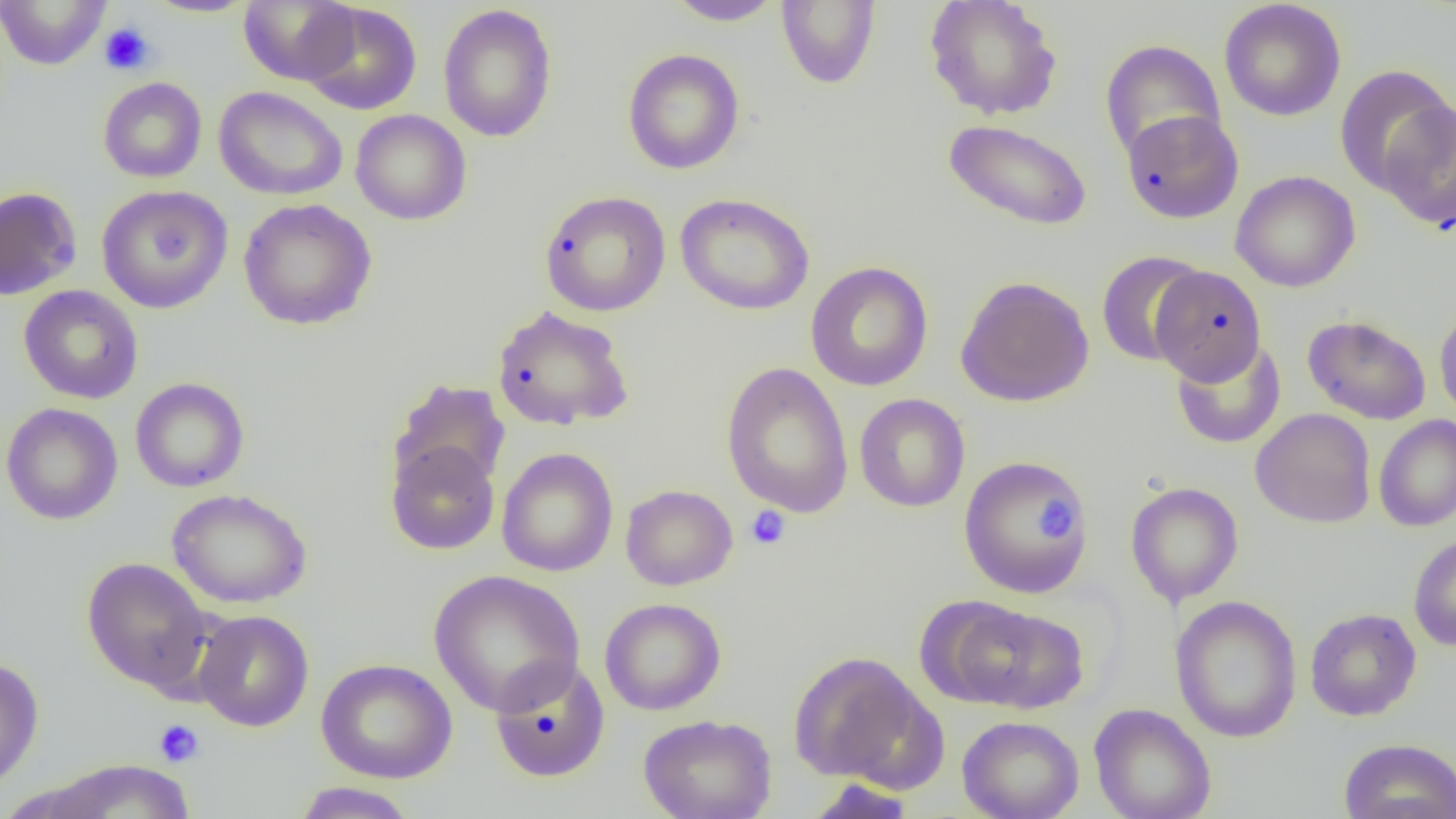

Summary:
  - Coordinate format: approximate bounding boxes as (x1, y1, x2, y2) in pixels
  - Uninfected red blood cell locations: (0, 0, 113, 70), (144, 0, 255, 17), (238, 0, 359, 85), (776, 0, 881, 90), (924, 0, 1063, 121), (665, 1, 786, 26), (1218, 1, 1347, 122), (299, 3, 422, 115), (438, 5, 558, 143), (1099, 39, 1226, 162), (622, 48, 745, 175), (1334, 64, 1454, 196), (97, 76, 207, 183), (214, 86, 348, 201), (1380, 101, 1456, 232), (350, 109, 472, 225), (1121, 110, 1244, 224), (942, 119, 1093, 232), (1230, 170, 1361, 292), (96, 185, 233, 313), (0, 186, 82, 301), (540, 191, 671, 317), (674, 193, 815, 316), (238, 198, 377, 330), (1096, 250, 1208, 367), (805, 261, 933, 391), (1151, 264, 1266, 385), (955, 276, 1094, 407), (18, 285, 143, 404), (1434, 304, 1456, 423), (491, 305, 635, 431), (1302, 314, 1432, 425), (1170, 337, 1286, 450), (721, 362, 853, 518), (130, 377, 249, 493), (388, 379, 510, 493), (854, 393, 970, 512), (1, 403, 123, 525), (1250, 408, 1377, 528), (1373, 414, 1456, 532), (385, 440, 500, 555), (497, 447, 618, 577), (958, 455, 1093, 599), (1126, 481, 1244, 607), (620, 484, 738, 591), (167, 488, 312, 608), (1408, 532, 1456, 651), (82, 557, 212, 693), (428, 569, 585, 716), (1170, 595, 1303, 743), (600, 598, 726, 716), (951, 602, 1089, 713), (1305, 607, 1421, 722), (192, 609, 314, 731), (787, 650, 932, 785), (0, 656, 45, 793), (316, 658, 457, 783), (489, 658, 611, 782), (1089, 704, 1216, 819), (638, 713, 777, 819), (958, 715, 1084, 819), (1338, 738, 1456, 819), (41, 759, 197, 818), (802, 779, 916, 818), (291, 782, 420, 818)
  - Platelet locations: (99, 22, 156, 76), (1036, 497, 1081, 540), (745, 505, 791, 551), (153, 719, 204, 768)
  - Slide-level diagnosis: negative for blood parasites
  - Magnification: 1000x
  - Modality: optical microscopy
  - Image size: 1456×819 pixels
  - Preparation: thin blood film
  - Field of view: single